Classify this cell by malaria status.
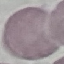

Uninfected.

Thin blood smear. Giemsa-stained preparation. Automatically extracted cell patch, resized to 64 × 64 pixels. Photographed with a smartphone camera at the microscope eyepiece.